Locate every blood parasite and identify its species.
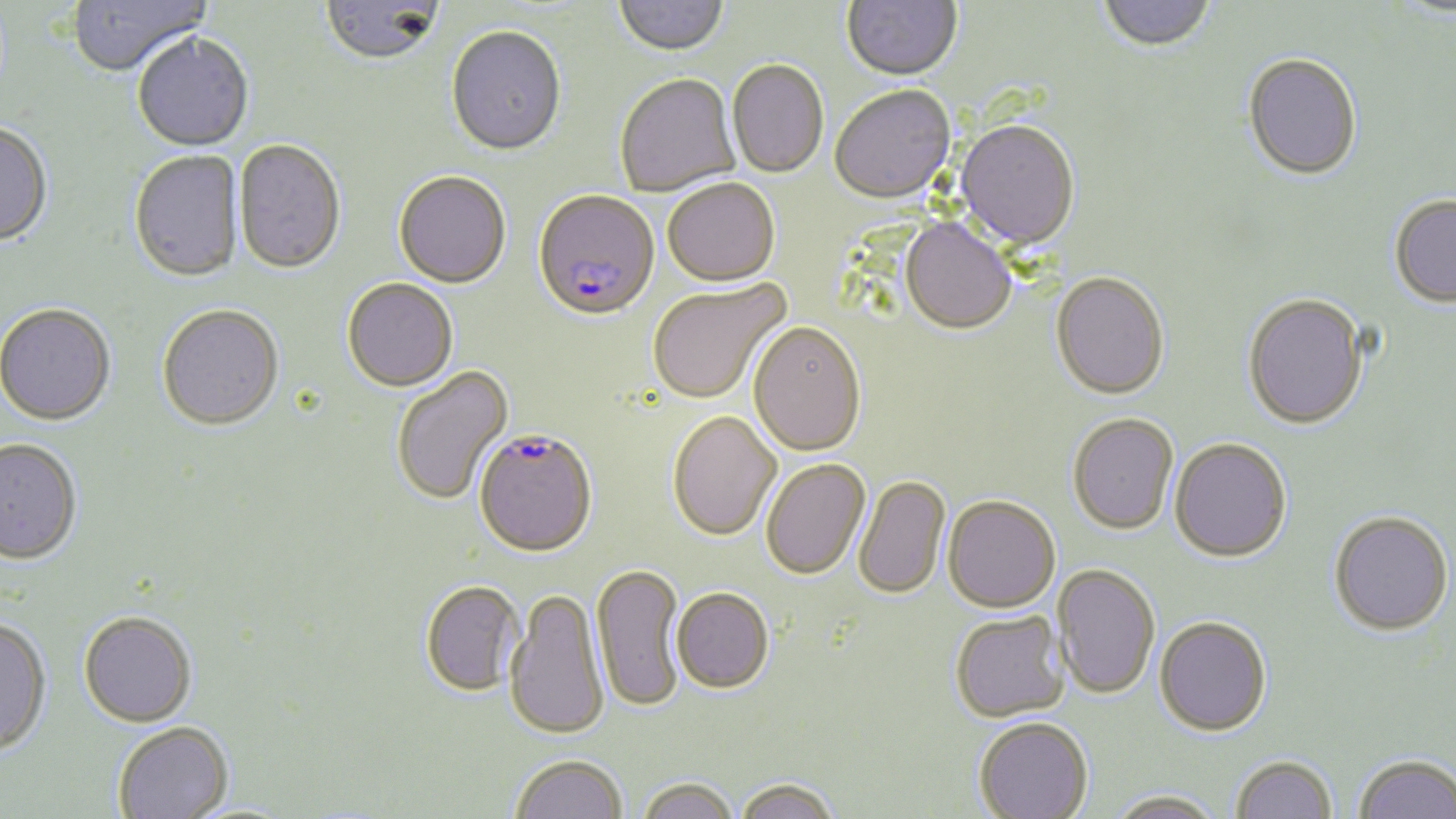

Approximate bounding boxes as (x1, y1, x2, y2) in pixels.
Plasmodium falciparum-infected red blood cells: (533, 193, 660, 324), (474, 431, 598, 560).
No Plasmodium ovale, Plasmodium malariae, Plasmodium vivax, Babesia divergens, or Trypanosoma brucei observed.

slide-level diagnosis = Plasmodium falciparum
image size = 1456×819 pixels
magnification = 1000x
preparation = thin blood smear
field of view = single
modality = light microscopy
uninfected red blood cell locations = approximate bounding boxes as (x1, y1, x2, y2) in pixels: (67, 0, 210, 79), (614, 0, 727, 58), (842, 0, 962, 83), (1098, 0, 1216, 55), (320, 1, 443, 69), (445, 28, 567, 159), (132, 34, 255, 154), (1243, 55, 1362, 182), (727, 61, 828, 180), (615, 76, 740, 199), (829, 87, 956, 208), (955, 122, 1080, 251), (0, 123, 53, 249), (234, 141, 346, 277), (128, 152, 244, 284), (394, 173, 511, 290), (663, 180, 780, 290), (1389, 195, 1456, 308), (899, 219, 1016, 337), (1051, 275, 1170, 402), (342, 280, 458, 393), (648, 281, 791, 406), (1243, 294, 1369, 430), (0, 306, 116, 428), (156, 306, 284, 432), (748, 324, 866, 458), (391, 366, 514, 507), (667, 413, 782, 543), (1067, 415, 1179, 537), (0, 439, 82, 567), (1169, 439, 1293, 564), (761, 460, 870, 581), (854, 476, 951, 601), (943, 498, 1060, 615), (1329, 510, 1453, 635), (591, 564, 685, 713), (1052, 564, 1160, 700), (421, 582, 526, 699), (505, 589, 609, 741), (672, 590, 774, 695), (78, 611, 197, 727), (950, 612, 1068, 724), (1154, 617, 1272, 737), (0, 618, 52, 755), (974, 719, 1094, 819), (113, 722, 234, 819), (1353, 753, 1456, 819), (510, 754, 628, 819), (1230, 754, 1338, 818), (637, 777, 738, 819), (734, 777, 841, 819), (1107, 790, 1226, 819)
stain = May-Grünwald-Giemsa